Assess the morphology of the erythrocytes.
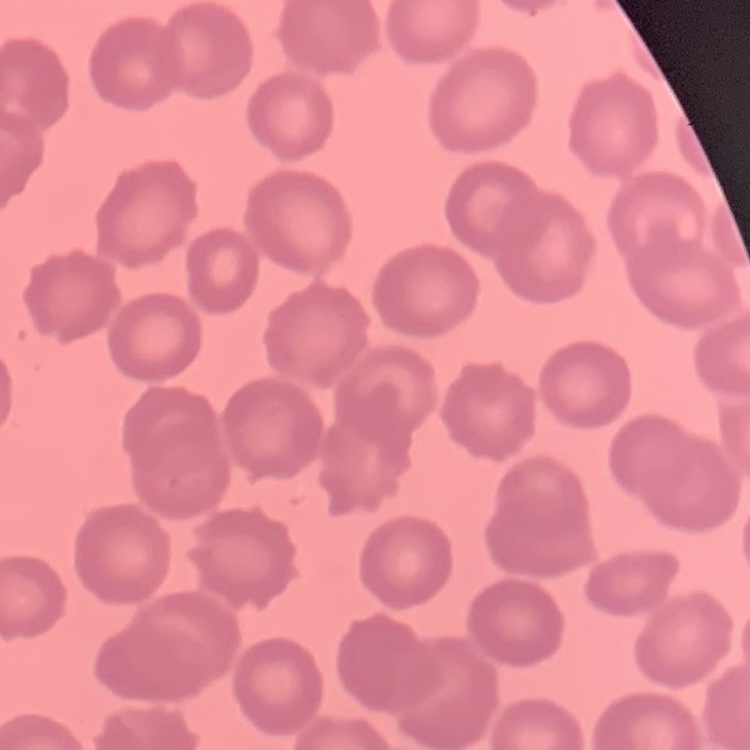

They show no rouleaux formation.

image type = one tile cut from a larger photomicrograph
preparation = thin blood film
stain = Field's or Giemsa